Locate every uninfected red blood cell.
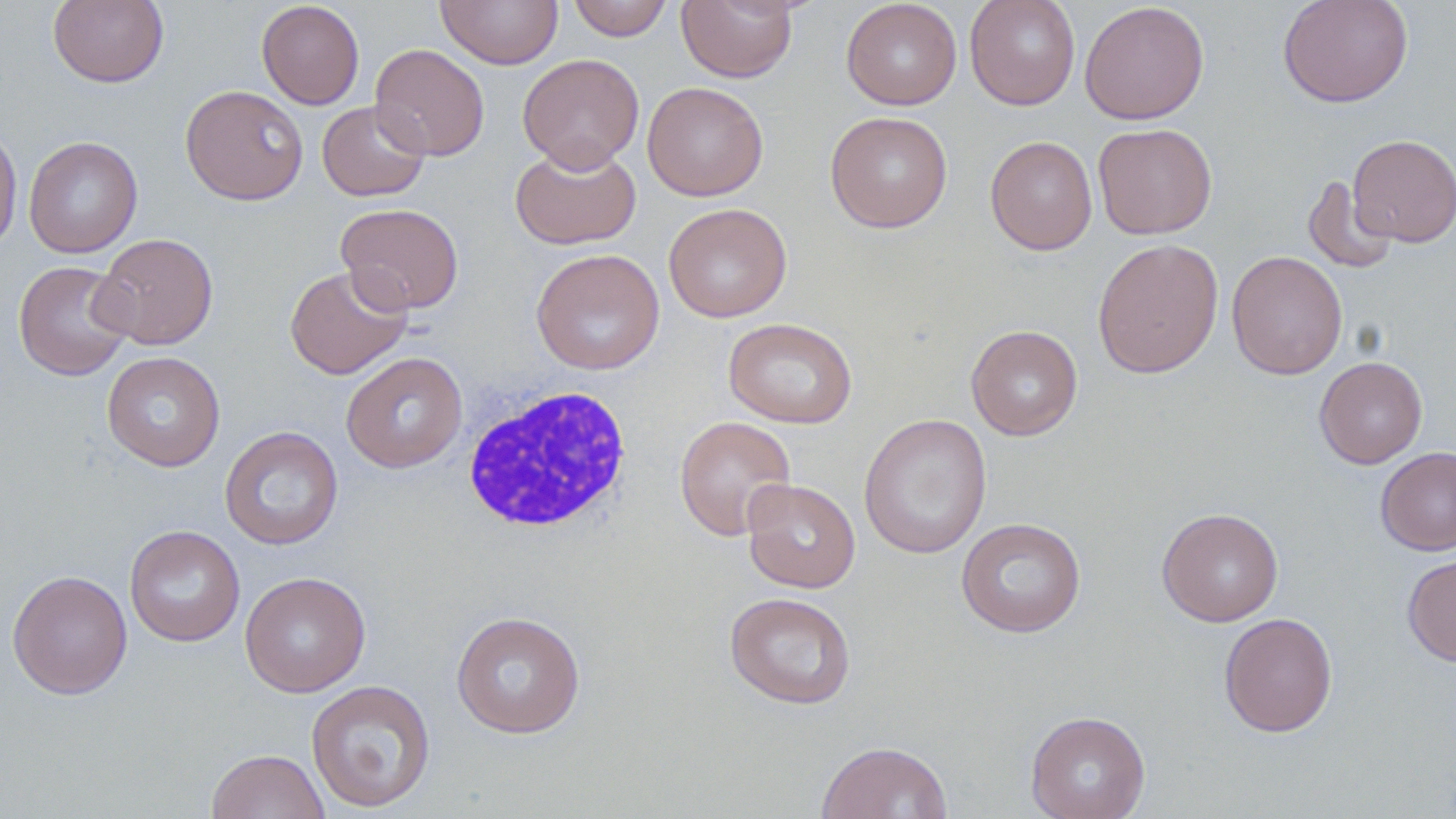

Approximate bounding boxes as [x1, y1, x2, y2] in pixels.
Uninfected red blood cells: [48, 0, 169, 88], [435, 0, 563, 69], [567, 0, 673, 41], [676, 0, 798, 83], [841, 0, 962, 110], [964, 0, 1081, 110], [1277, 0, 1414, 108], [256, 1, 365, 110], [1080, 2, 1209, 125], [369, 43, 489, 161], [518, 54, 644, 173], [642, 82, 768, 201], [179, 84, 309, 205], [317, 100, 430, 202], [824, 111, 953, 233], [1093, 123, 1218, 240], [0, 125, 23, 255], [1347, 134, 1456, 247], [985, 135, 1097, 255], [23, 136, 143, 258], [510, 143, 642, 250], [1302, 176, 1399, 274], [335, 202, 464, 315], [663, 203, 792, 323], [93, 232, 219, 350], [1092, 238, 1224, 379], [531, 248, 665, 375], [1227, 251, 1348, 380], [13, 259, 136, 381], [284, 265, 413, 379], [723, 317, 858, 428], [966, 324, 1083, 441], [102, 351, 226, 471], [340, 352, 468, 473], [1314, 356, 1427, 469], [858, 413, 992, 559], [674, 415, 797, 541], [219, 425, 344, 550], [1376, 447, 1456, 555], [742, 479, 860, 593], [1156, 507, 1283, 626], [956, 517, 1086, 638], [124, 524, 245, 647], [1402, 553, 1456, 666], [7, 569, 133, 699], [240, 571, 371, 697], [724, 592, 857, 709], [450, 610, 586, 738], [1219, 612, 1338, 737], [306, 678, 436, 812], [1025, 711, 1151, 819], [815, 741, 953, 819], [207, 749, 329, 819].

{
  "slide_level_diagnosis": "no evidence of blood parasites",
  "field_of_view": "single",
  "preparation": "thin blood smear",
  "white_blood_cell_locations": "approximate bounding boxes as [x1, y1, x2, y2] in pixels: [461, 383, 634, 535]",
  "stain": "May-Grünwald-Giemsa",
  "image_size": "1456×819 pixels",
  "magnification": "1000x",
  "modality": "optical microscopy"
}